State the blood parasite species.
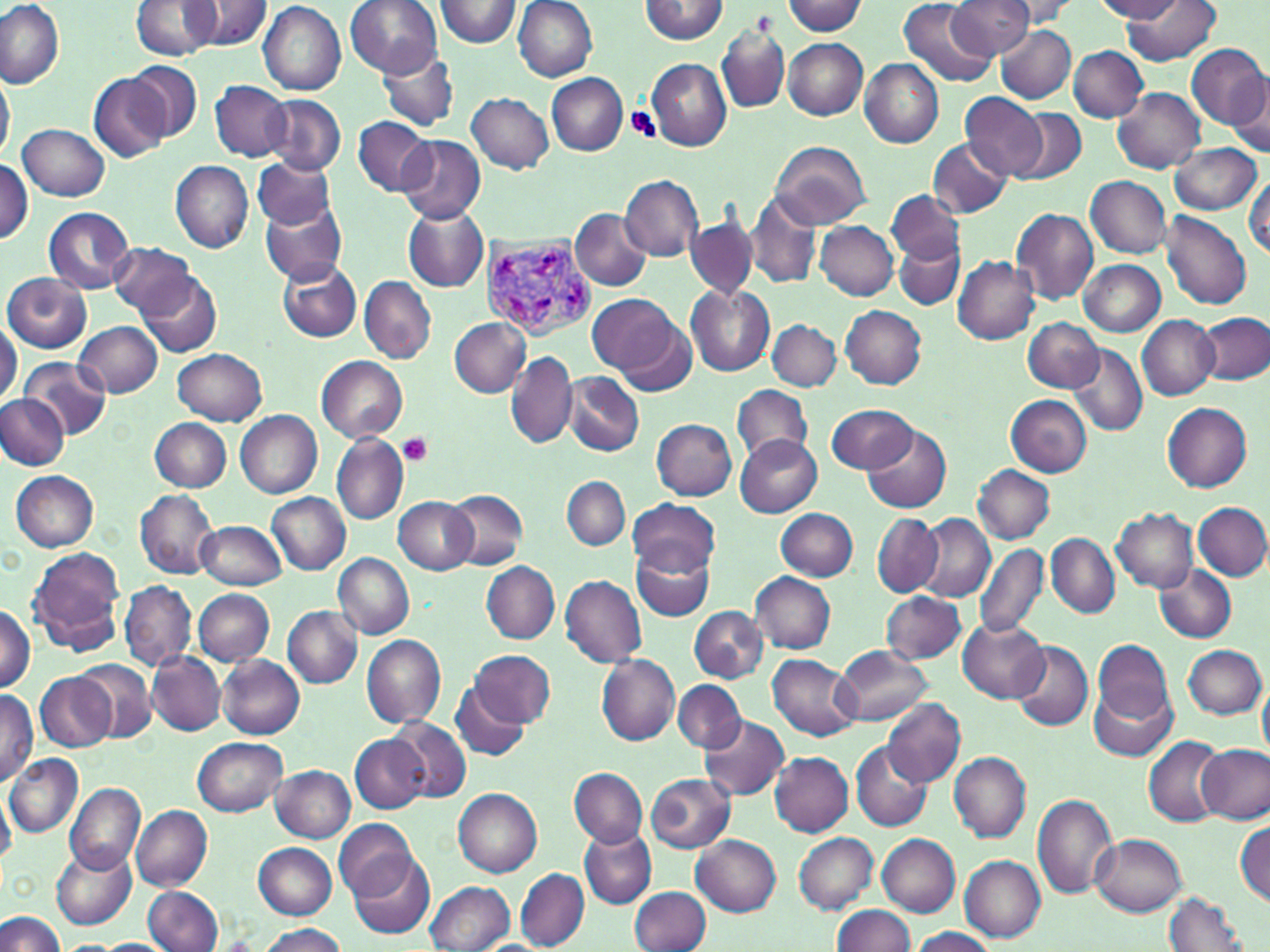
Plasmodium vivax.

Approximate bounding boxes as [x1, y1, x2, y2] in pixels. Platelet locations: [627, 105, 662, 143], [398, 433, 434, 466]. Uninfected red blood cell locations: [0, 0, 66, 88], [187, 0, 272, 51], [344, 0, 442, 77], [437, 0, 521, 47], [513, 0, 599, 81], [642, 0, 729, 44], [947, 0, 1033, 59], [998, 0, 1080, 26], [1094, 0, 1184, 21], [132, 1, 220, 60], [899, 1, 994, 86], [1123, 1, 1222, 66], [258, 2, 346, 95], [782, 2, 865, 35], [717, 20, 790, 116], [997, 24, 1075, 104], [783, 38, 868, 120], [1187, 44, 1268, 128], [1069, 46, 1148, 122], [375, 48, 461, 134], [860, 57, 944, 148], [647, 59, 731, 150], [129, 60, 203, 140], [0, 65, 14, 166], [89, 73, 171, 161], [546, 73, 627, 156], [210, 81, 290, 161], [1229, 82, 1269, 157], [1112, 87, 1204, 174], [467, 93, 553, 173], [961, 93, 1048, 178], [263, 94, 346, 177], [1014, 109, 1086, 185], [353, 116, 435, 195], [19, 124, 109, 200], [396, 134, 485, 225], [929, 138, 1012, 218], [770, 141, 873, 229], [1169, 143, 1261, 214], [750, 147, 846, 276], [253, 155, 334, 229], [0, 160, 33, 243], [170, 160, 253, 252], [1245, 172, 1269, 260], [622, 176, 703, 261], [1084, 176, 1172, 258], [744, 191, 821, 290], [887, 191, 965, 268], [260, 199, 347, 285], [402, 206, 489, 293], [570, 206, 651, 290], [43, 208, 134, 293], [1011, 209, 1098, 306], [1161, 211, 1251, 309], [687, 215, 758, 299], [815, 221, 897, 299], [893, 236, 965, 310], [107, 242, 195, 318], [953, 255, 1041, 343], [1079, 259, 1166, 336], [279, 262, 361, 341], [140, 273, 221, 357], [3, 274, 91, 354], [360, 276, 436, 364], [686, 285, 774, 376], [589, 293, 677, 375], [841, 306, 926, 389], [1198, 312, 1270, 385], [616, 313, 696, 396], [1137, 315, 1220, 399], [1024, 317, 1104, 392], [448, 318, 531, 397], [768, 319, 841, 391], [0, 320, 21, 410], [75, 321, 162, 398], [1068, 342, 1147, 437], [172, 347, 267, 425], [507, 352, 576, 449], [316, 355, 408, 442], [22, 357, 112, 438], [565, 373, 644, 456], [731, 384, 814, 466], [3, 394, 79, 546], [0, 395, 69, 469], [1006, 395, 1092, 475], [1162, 401, 1252, 491], [826, 404, 917, 473], [235, 410, 322, 497], [651, 417, 737, 500], [150, 418, 232, 491], [862, 424, 952, 514], [331, 434, 407, 525], [735, 435, 821, 517], [972, 465, 1053, 543], [11, 470, 99, 551], [562, 475, 630, 550], [445, 488, 527, 569], [135, 490, 219, 578], [267, 492, 351, 575], [393, 497, 478, 574], [628, 498, 718, 576], [1193, 503, 1270, 580], [1112, 507, 1198, 593], [776, 508, 857, 581], [872, 514, 942, 596], [917, 514, 995, 602], [196, 520, 285, 591], [1046, 533, 1119, 618], [632, 542, 716, 623], [973, 543, 1048, 640], [27, 547, 126, 653], [333, 552, 414, 639], [482, 561, 560, 642], [1155, 563, 1237, 643], [751, 573, 835, 652], [561, 575, 647, 668], [117, 581, 195, 671], [194, 589, 275, 665], [882, 591, 966, 664], [0, 602, 35, 692], [283, 606, 362, 687], [689, 606, 768, 682], [959, 617, 1050, 702], [359, 633, 445, 728], [1093, 640, 1173, 723], [1011, 641, 1094, 733], [1183, 645, 1266, 719], [833, 646, 930, 725], [471, 648, 555, 727], [147, 651, 225, 735], [597, 653, 679, 745], [217, 655, 305, 739], [768, 655, 861, 741], [79, 660, 155, 740], [35, 672, 118, 750], [1258, 672, 1270, 764], [673, 680, 746, 753], [450, 681, 531, 762], [1090, 688, 1177, 760], [1, 690, 38, 782], [882, 698, 965, 787], [697, 715, 790, 803], [389, 718, 470, 803], [351, 734, 430, 813], [1144, 736, 1228, 826], [193, 737, 288, 816], [851, 743, 933, 832], [1198, 744, 1269, 825], [771, 752, 853, 836], [949, 752, 1030, 843], [5, 754, 82, 839], [272, 765, 355, 842], [569, 766, 647, 848], [646, 773, 736, 852], [66, 783, 145, 876], [454, 788, 543, 877], [0, 791, 15, 867], [1031, 793, 1117, 898], [130, 804, 213, 890], [1235, 819, 1270, 907], [333, 820, 422, 904], [579, 826, 655, 909], [793, 832, 878, 913], [1091, 834, 1187, 916], [692, 835, 781, 915], [877, 835, 960, 916], [252, 842, 338, 921], [53, 846, 136, 929], [347, 848, 435, 940], [960, 856, 1046, 941], [516, 868, 589, 951], [425, 881, 514, 952], [143, 885, 224, 952], [631, 886, 711, 951], [1164, 893, 1250, 952], [832, 905, 916, 952], [0, 910, 66, 952], [256, 923, 347, 952], [908, 927, 998, 951], [95, 938, 173, 951]. Plasmodium vivax-infected red blood cell locations: [476, 238, 596, 342]. Thin blood smear. Single field of view. May-Grünwald-Giemsa-stained preparation. Image is 1270×952 pixels. Captured at 1000x magnification. Optical microscopy.